Locate every parasitized red blood cell.
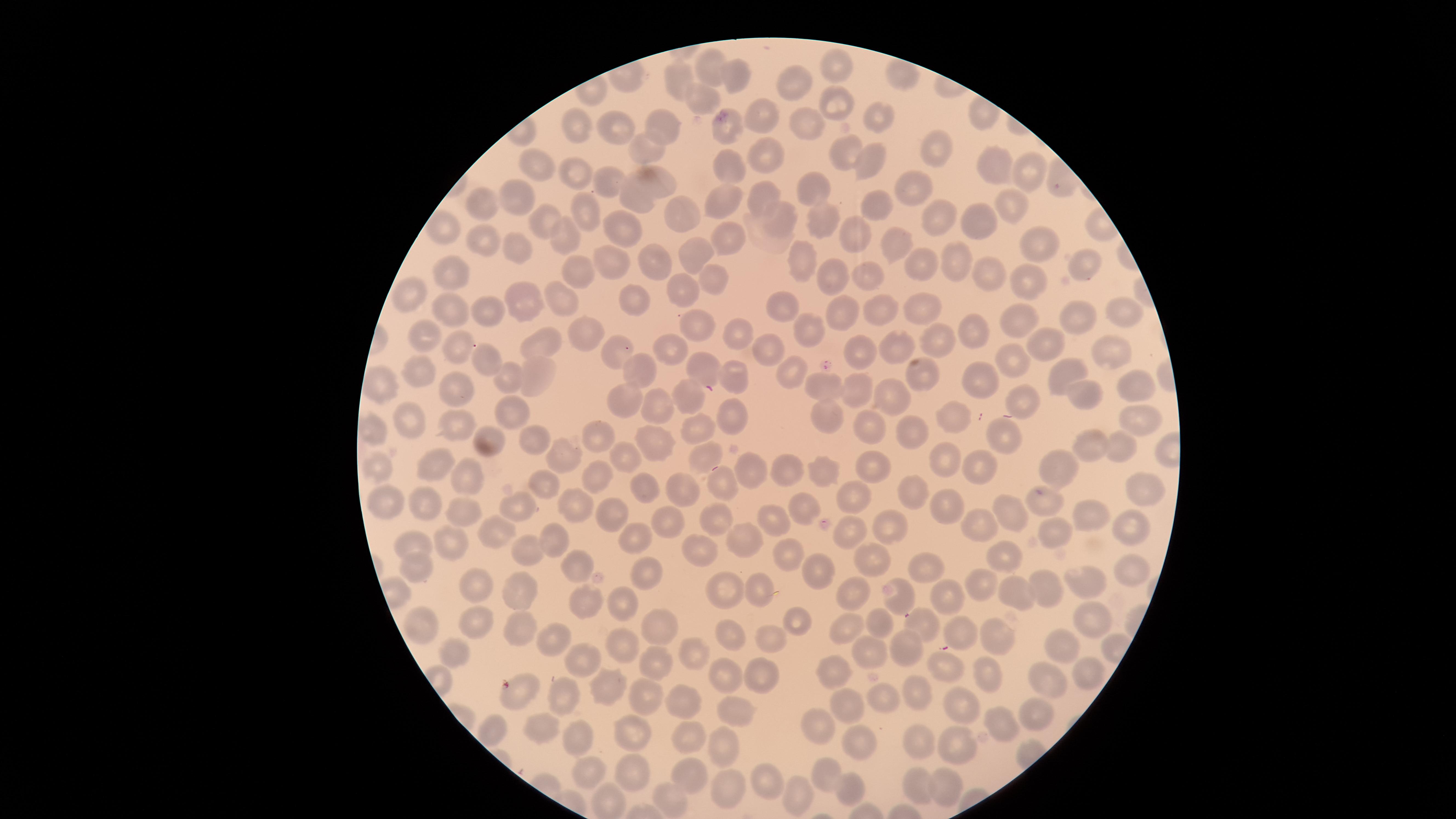

No parasitized red blood cells identified.

Approximate marker points as [x, y] in pixels. Uninfected red blood cells: [706, 68], [832, 70], [737, 78], [795, 81], [679, 82], [699, 98], [829, 101], [760, 112], [873, 117], [803, 119], [661, 128], [575, 130], [723, 131], [615, 134], [641, 147], [847, 154], [940, 154], [766, 157], [869, 164], [991, 164], [533, 165], [730, 166], [1030, 173], [576, 175], [607, 180], [662, 184], [810, 190], [915, 190], [756, 197], [517, 198], [642, 201], [486, 204], [723, 204], [869, 204], [1012, 207], [588, 211], [674, 215], [542, 220], [775, 220], [938, 222], [817, 223], [984, 223], [623, 229], [722, 233], [563, 237], [855, 239], [899, 241], [1036, 243], [478, 246], [517, 248], [699, 255], [953, 259], [801, 263], [1081, 263], [611, 264], [654, 264], [919, 264], [976, 269], [577, 274], [458, 277], [828, 277], [859, 277], [714, 279], [1025, 281], [682, 294], [634, 295], [406, 298], [559, 298], [526, 302], [782, 307], [447, 309], [489, 310], [1123, 310], [882, 311], [921, 311], [843, 315], [1073, 317], [691, 320], [1023, 324], [730, 331], [972, 332], [810, 333], [421, 334], [578, 334], [539, 340], [1045, 340], [931, 342], [671, 346], [893, 346], [858, 349], [460, 350], [611, 350], [1111, 350], [768, 352], [1004, 358], [487, 364], [638, 367], [414, 370], [704, 372], [790, 373], [1068, 373], [539, 375], [737, 375], [916, 378], [509, 379], [975, 379], [1139, 383], [456, 388], [857, 388], [819, 389], [630, 397], [689, 397], [890, 397], [1084, 399], [1021, 400], [656, 406], [511, 410], [734, 417], [407, 418], [828, 418], [947, 420], [1138, 420], [454, 429], [697, 430], [868, 430], [371, 432], [1003, 433], [491, 434], [594, 434], [914, 435], [530, 440], [1088, 445], [1119, 446], [653, 450], [567, 454], [627, 460], [699, 460], [947, 463], [980, 463], [438, 466], [1064, 467], [869, 469], [378, 471], [752, 471], [823, 472], [786, 473], [600, 474], [469, 479], [545, 484], [1143, 484], [716, 485], [637, 489], [682, 489], [911, 491], [385, 494], [851, 498], [802, 504], [944, 504], [1048, 504], [428, 506], [574, 507], [517, 509], [1005, 511], [607, 513], [468, 514], [1084, 514], [668, 519], [721, 520], [777, 524], [886, 527], [980, 527], [1132, 527], [1055, 529], [844, 533], [636, 534], [503, 536], [550, 537], [745, 538], [447, 544], [416, 546], [693, 548], [525, 550], [787, 553], [872, 556], [1004, 557], [573, 565], [643, 566], [917, 566], [413, 568], [823, 571], [1131, 573], [478, 584], [1087, 584], [979, 586], [1043, 588], [520, 589], [724, 589], [1014, 592], [759, 594], [852, 594], [948, 598], [901, 601], [581, 603], [622, 603], [1094, 616], [801, 620], [475, 623], [657, 623], [846, 624], [884, 624], [420, 625], [518, 628], [923, 629], [957, 629], [549, 636], [735, 636], [997, 638], [772, 639], [1062, 644], [908, 649], [629, 650], [869, 652], [452, 654], [696, 656], [580, 662], [658, 663], [943, 667], [835, 670], [988, 671], [1088, 672], [726, 677], [760, 677], [611, 685], [1050, 685], [566, 691], [912, 691], [521, 693], [651, 696], [880, 701], [688, 702], [962, 706], [847, 708], [735, 712], [1036, 715], [1000, 724], [534, 727], [814, 729], [631, 732], [491, 733], [578, 733], [686, 736], [917, 740], [724, 746], [858, 747], [956, 748], [627, 768], [590, 771], [823, 772], [688, 773], [771, 784], [942, 784], [916, 785], [848, 786], [725, 787], [795, 794], [670, 797], [608, 800]. Thin blood film. Giemsa stain. Image is 1456×819 pixels. The visible region is circular. Single field of view. Smartphone photograph through the microscope eyepiece.